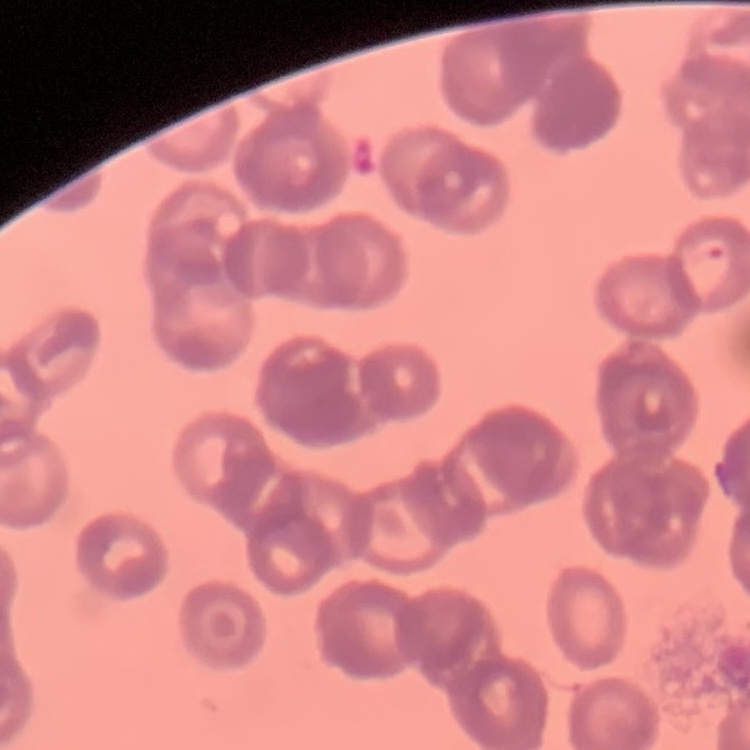 The red blood cells show rouleaux formation. Thin blood smear. Stained with either Field's or Giemsa. One tile cut from a larger photomicrograph.